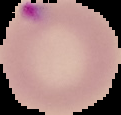
preparation = thin blood film
malaria status = parasitized
image type = segmented cell region on a black background
image size = 121×115 pixels